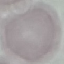

Summary:
  - Result: negative for malaria parasites
  - Stain: Giemsa
  - Image type: cell patch, automatically extracted from a larger field of view and resized to 64 × 64 pixels
  - Capture: smartphone through the microscope eyepiece
  - Preparation: thin blood smear